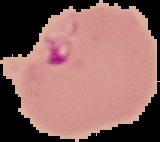

Summary:
  - Image type: segmented cell region with the area outside set to black
  - Preparation: thin blood film
  - Image size: 160×142 pixels
  - Result: malaria parasites detected